Name the parasite shown.
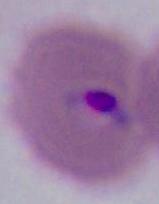
Plasmodium.

magnification = 400x or 1000x
modality = micrograph